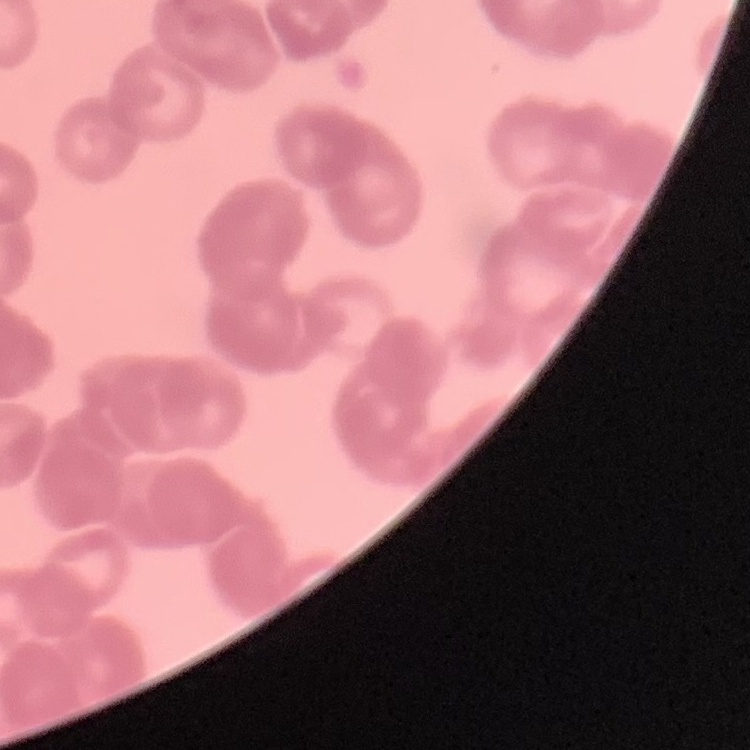

Summary:
  - Red blood cell morphology: rouleaux formation
  - Preparation: thin blood film
  - Image type: one tile cut from a larger photomicrograph
  - Stain: Field's or Giemsa